Locate every blood parasite and identify its species.
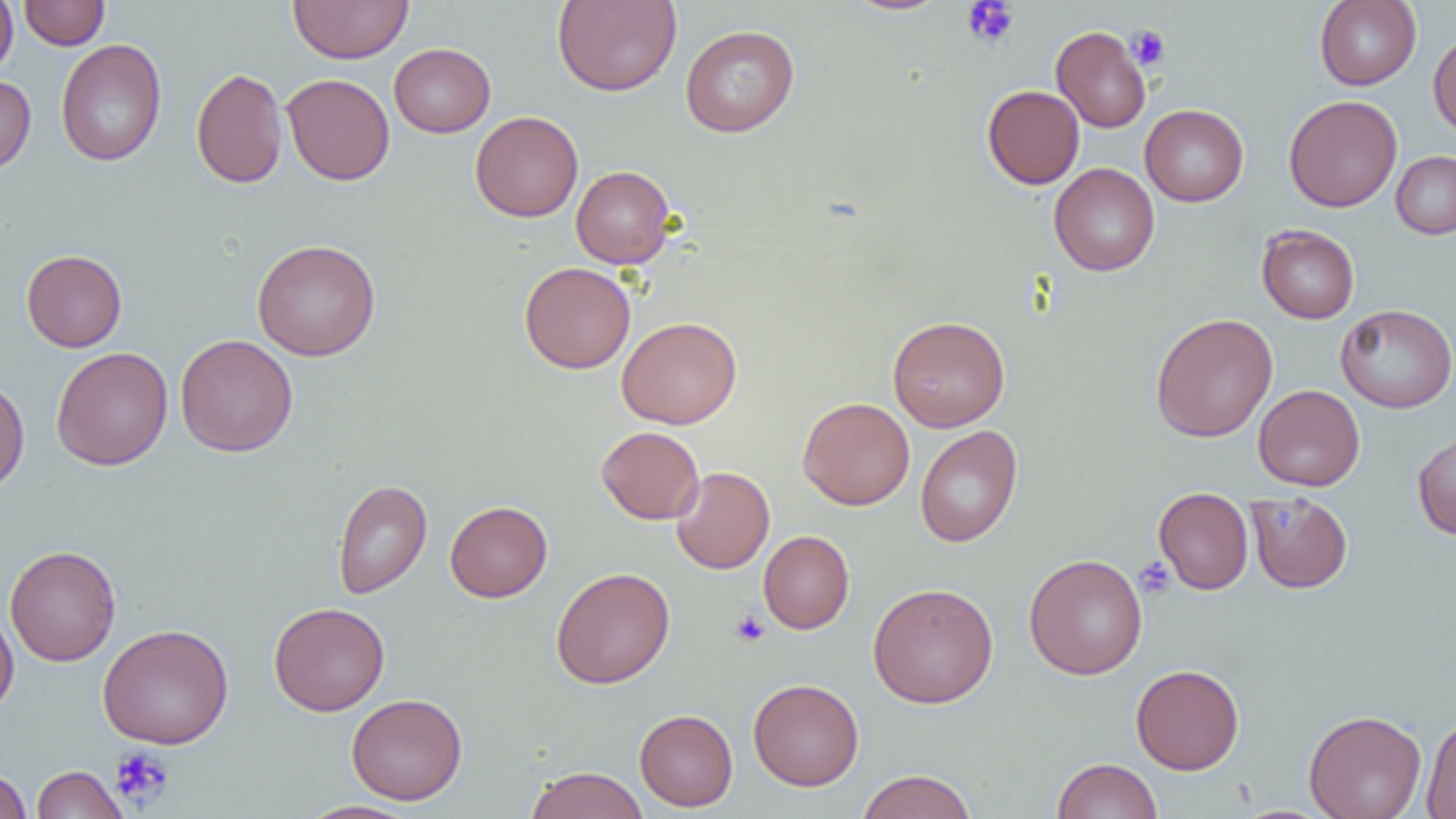

No blood parasites seen.

Approximate bounding boxes as [x1, y1, x2, y2] in pixels. Uninfected red blood cell locations: [0, 0, 18, 80], [19, 0, 109, 50], [288, 0, 413, 64], [552, 0, 681, 96], [843, 0, 952, 16], [1314, 0, 1421, 90], [680, 24, 799, 137], [1051, 26, 1150, 133], [1428, 30, 1456, 138], [55, 39, 167, 167], [389, 43, 495, 137], [191, 67, 288, 188], [282, 73, 394, 186], [0, 75, 36, 176], [982, 85, 1084, 189], [1284, 95, 1402, 212], [1140, 104, 1248, 206], [470, 110, 583, 222], [1391, 150, 1456, 239], [1049, 163, 1159, 276], [571, 165, 675, 268], [1257, 225, 1360, 323], [251, 239, 381, 361], [21, 249, 127, 352], [519, 262, 636, 373], [1335, 304, 1456, 413], [1150, 313, 1278, 442], [887, 315, 1010, 432], [616, 316, 742, 429], [175, 333, 298, 457], [51, 347, 173, 470], [0, 377, 29, 495], [1253, 384, 1365, 491], [798, 397, 915, 510], [915, 425, 1022, 548], [597, 426, 704, 524], [1412, 427, 1456, 540], [672, 466, 774, 574], [333, 479, 432, 599], [1153, 487, 1254, 595], [1246, 492, 1353, 593], [445, 500, 552, 602], [758, 530, 854, 634], [4, 544, 121, 667], [1024, 553, 1147, 680], [551, 567, 675, 689], [867, 582, 998, 708], [269, 601, 389, 716], [0, 606, 19, 718], [98, 623, 234, 749], [1131, 664, 1244, 774], [748, 678, 864, 790], [346, 693, 468, 805], [634, 709, 738, 811], [1304, 709, 1426, 819], [1422, 717, 1456, 818], [1052, 758, 1162, 819], [31, 765, 128, 818], [525, 766, 649, 819], [0, 767, 32, 819], [856, 769, 977, 819], [299, 800, 419, 818]. Platelet locations: [961, 1, 1020, 48], [1127, 25, 1170, 70], [1134, 557, 1176, 599], [731, 610, 770, 646], [109, 747, 174, 808]. Slide-level diagnosis: no evidence of blood parasites. Light microscopy. 1000x magnification. Image is 1456×819 pixels. One field of a larger specimen. Thin blood film.